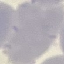

Summary:
  - Malaria status: uninfected
  - Stain: Giemsa
  - Image type: cell patch, automatically extracted from a larger field of view and resized to 64 × 64 pixels
  - Capture: smartphone camera at the microscope eyepiece
  - Preparation: thin blood smear